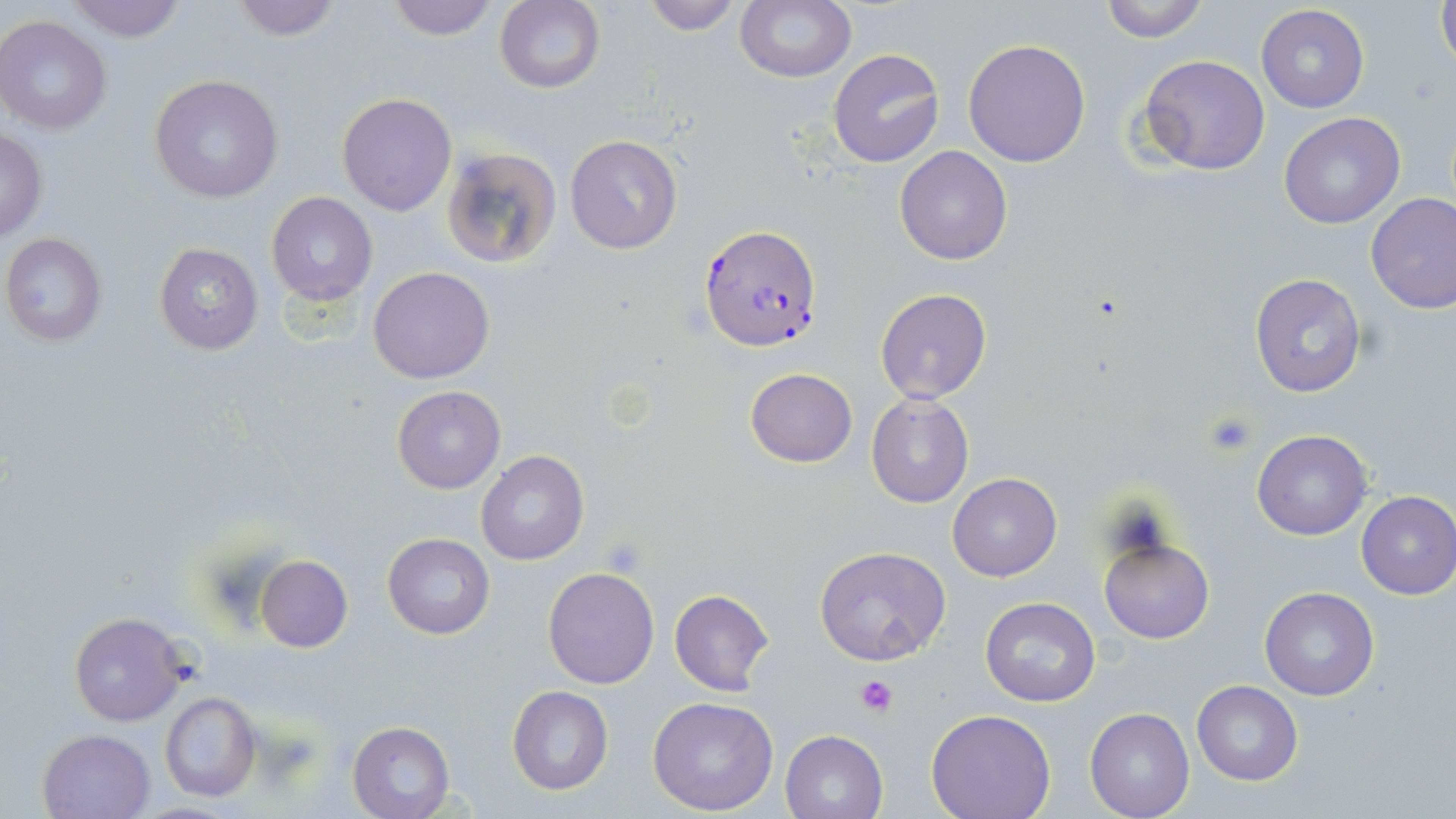
Summary:
  - Coordinate format: approximate bounding boxes as [x1, y1, x2, y2] in pixels
  - Platelet locations: [1203, 410, 1257, 458], [855, 676, 897, 717]
  - Plasmodium falciparum-infected red blood cell locations: [699, 222, 824, 354]
  - Uninfected red blood cell locations: [63, 0, 188, 43], [226, 0, 345, 42], [385, 0, 499, 40], [735, 0, 855, 82], [1433, 0, 1455, 78], [496, 1, 605, 94], [640, 1, 743, 34], [1096, 1, 1212, 42], [1256, 5, 1370, 113], [1, 16, 115, 135], [963, 39, 1091, 167], [830, 50, 944, 167], [1137, 54, 1270, 176], [147, 74, 285, 203], [336, 92, 458, 216], [1279, 112, 1405, 228], [0, 127, 48, 243], [565, 135, 683, 255], [894, 146, 1013, 265], [439, 147, 560, 271], [266, 192, 379, 306], [1366, 192, 1456, 313], [2, 233, 111, 347], [154, 241, 263, 354], [368, 265, 495, 384], [1247, 271, 1368, 398], [874, 289, 992, 405], [745, 367, 857, 467], [392, 386, 505, 493], [865, 393, 975, 510], [1252, 429, 1372, 541], [477, 451, 588, 566], [947, 472, 1062, 583], [1356, 490, 1456, 599], [383, 533, 495, 639], [1098, 536, 1216, 645], [814, 545, 951, 665], [255, 556, 353, 653], [543, 566, 659, 689], [1258, 586, 1379, 700], [668, 589, 775, 696], [979, 597, 1103, 707], [68, 610, 189, 726], [1191, 681, 1303, 785], [508, 685, 613, 795], [157, 691, 262, 803], [647, 696, 779, 815], [1085, 705, 1195, 819], [926, 711, 1056, 819], [348, 721, 456, 819], [37, 728, 154, 818], [779, 731, 888, 819]
  - Slide-level diagnosis: Plasmodium falciparum
  - Modality: light microscopy
  - Image size: 1456×819 pixels
  - Preparation: thin blood smear
  - Stain: May-Grünwald-Giemsa
  - Magnification: 1000x
  - Field of view: one of a larger specimen